Point out each Plasmodium parasite.
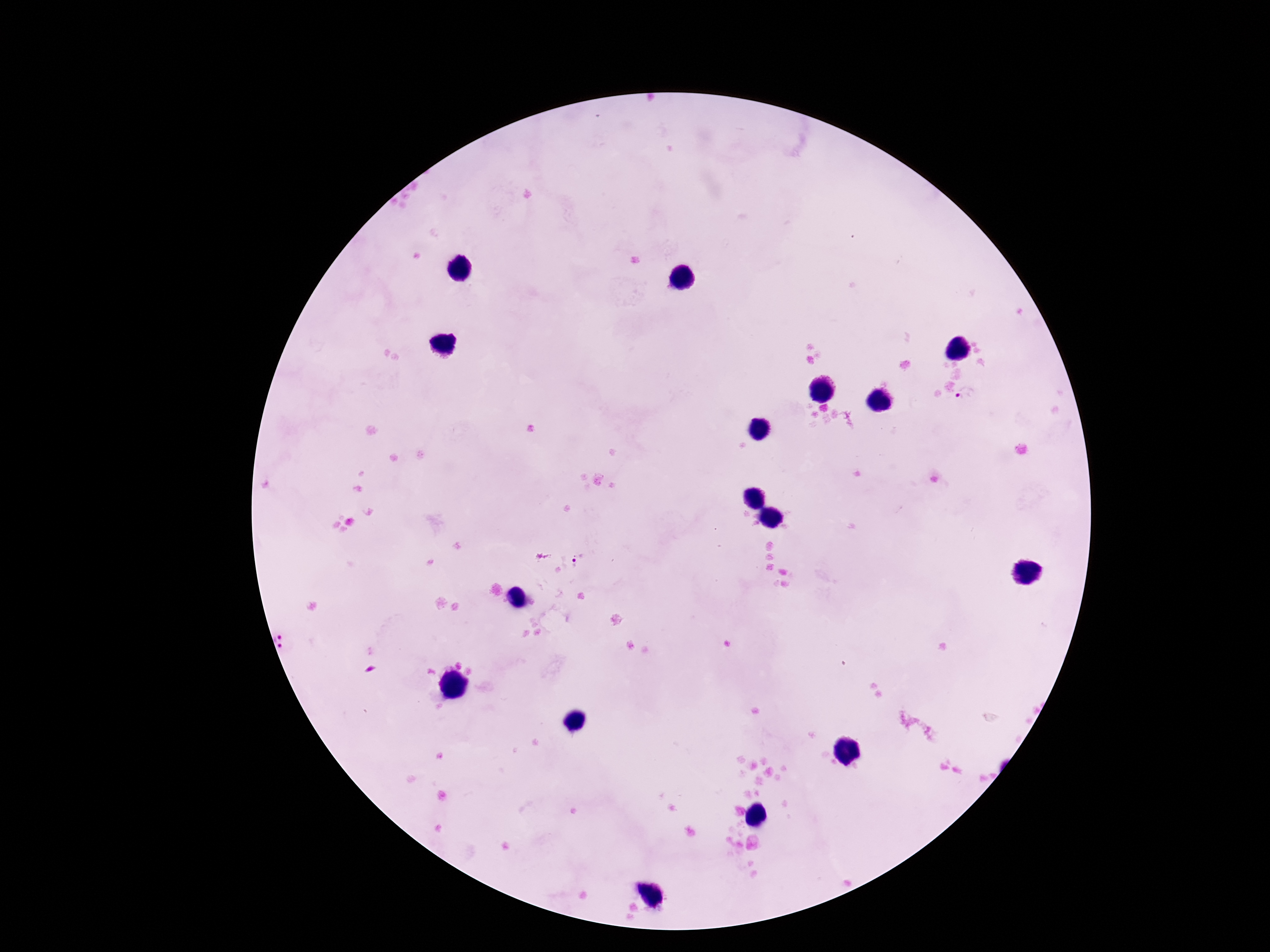

Approximate centers as [x, y] in pixels.
Plasmodium parasites: [969, 397], [570, 560], [292, 640].

Summary:
  - Image size: 1270×952 pixels
  - Capture: smartphone camera through the microscope eyepiece
  - Preparation: thick peripheral-blood smear
  - Field of view: single
  - Stain: Giemsa
  - Patient malaria status: positive
  - Magnification: 100x